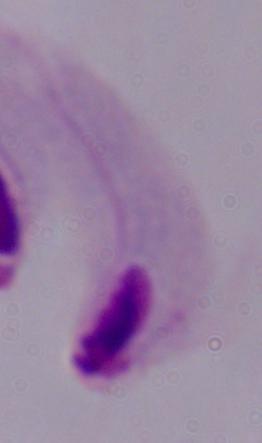

Summary:
  - Modality: photomicrograph
  - Magnification: 1000x
  - Identification: trichomonad